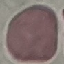

result: no malaria parasites seen
image_type: automatically extracted cell patch, resized to 64 × 64 pixels
stain: Giemsa
capture: smartphone camera at the microscope eyepiece
preparation: thin smear